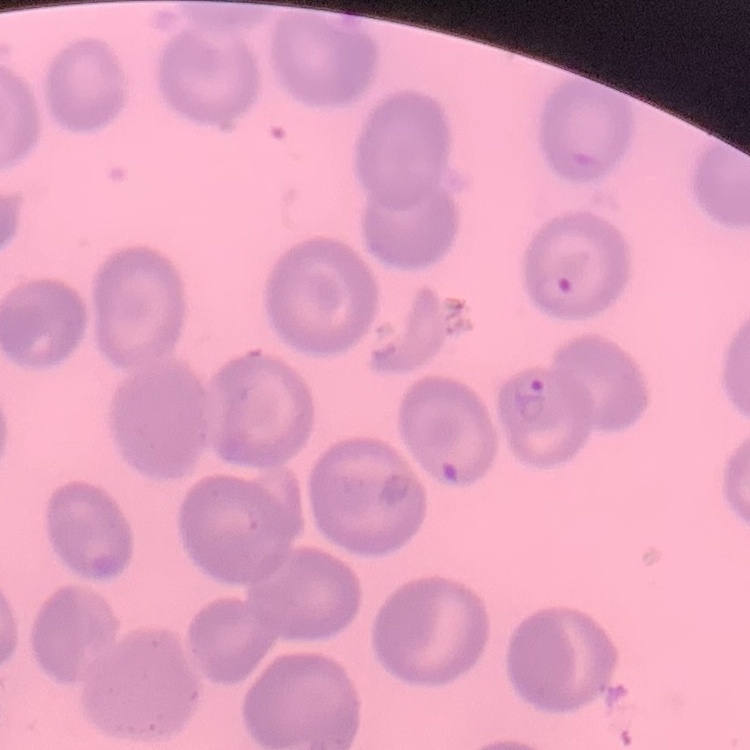

red blood cell morphology = no rouleaux formation
stain = Field's or Giemsa
preparation = thin peripheral smear
image type = one tile cut from a larger photomicrograph